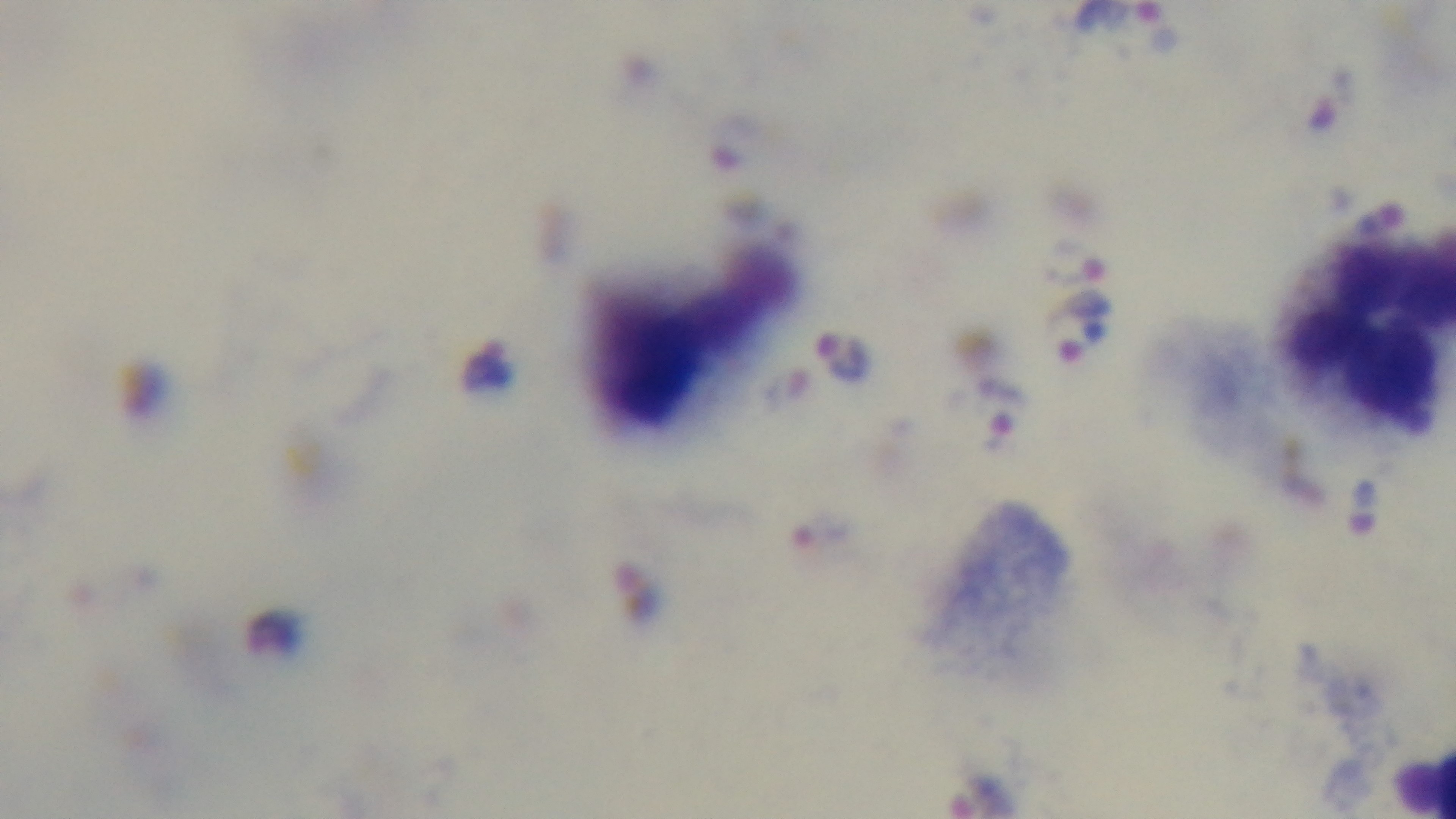
Giemsa stain. One field from the slide. Preparation: thick smear. Oil-immersion objective, 100x. Photomicrograph. Malaria status: positive. Mounted 4K digital camera.